Name the parasite shown.
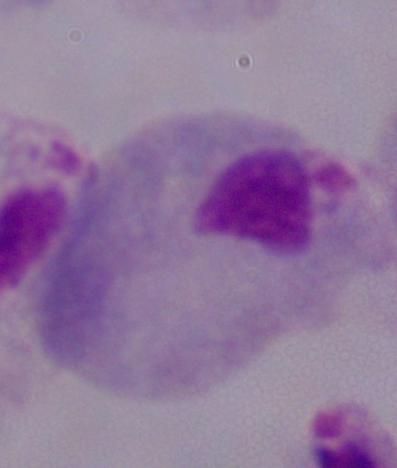

A trichomonad.

Summary:
  - Modality: micrograph
  - Magnification: 1000x